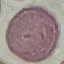
Summary:
  - Malaria status: uninfected
  - Preparation: thin blood film
  - Stain: Giemsa
  - Capture: smartphone through the microscope eyepiece
  - Image type: automatically extracted cell patch, resized to 64 × 64 pixels